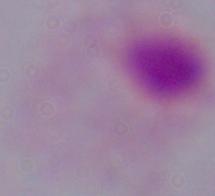
{
  "magnification": "1000x",
  "modality": "photomicrograph",
  "identification": "trichomonad"
}